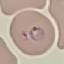 Malaria status: parasitized. Thin blood film. Giemsa stain. Automatically extracted cell patch, resized to 64 × 64 pixels. Acquired by smartphone through the microscope eyepiece.